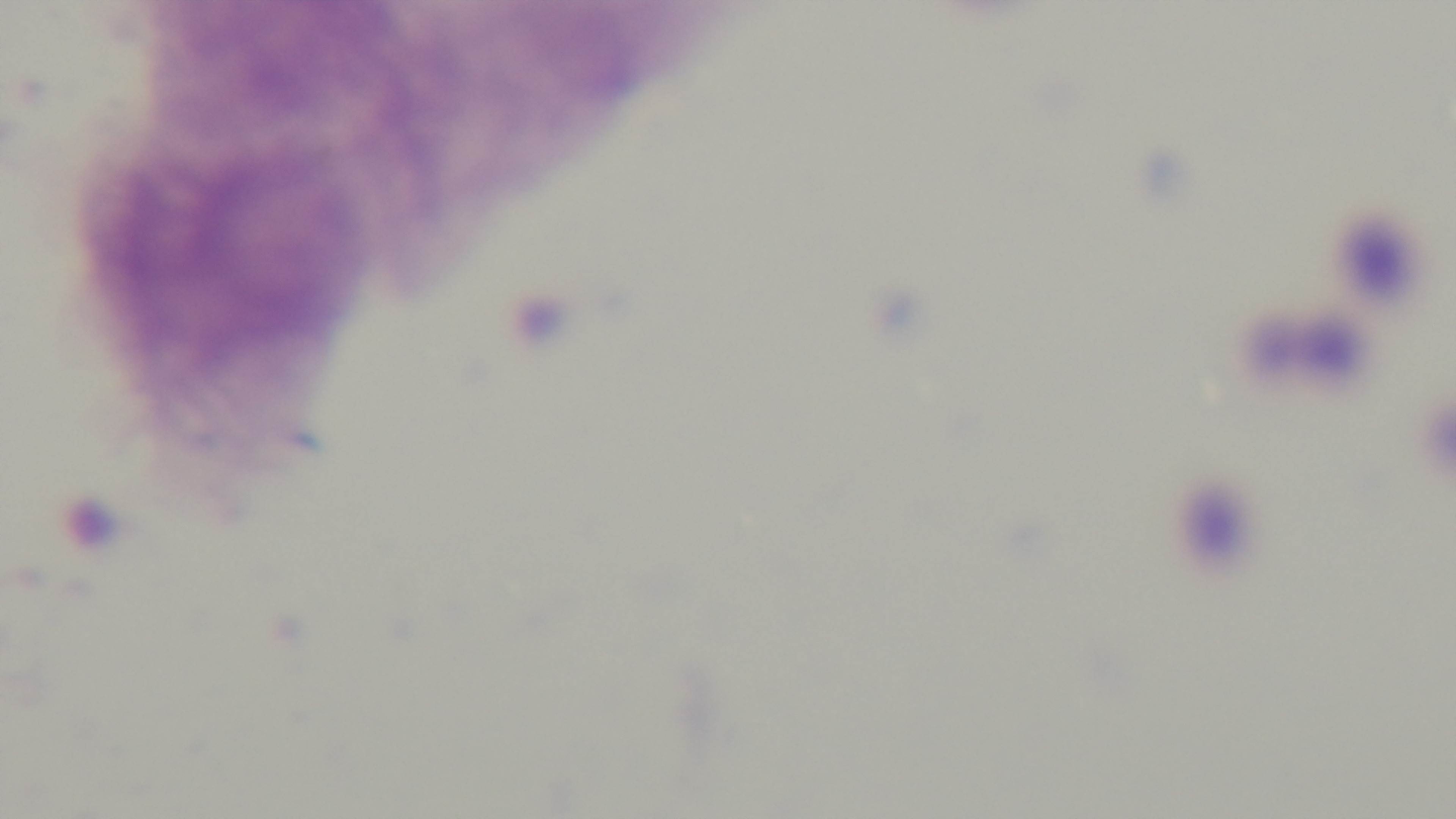
malaria status = uninfected
preparation = thick
objective = 100x oil immersion
stain = Giemsa
capture = mounted 4K digital camera
field of view = single
modality = light microscopy